Point out each Plasmodium parasite.
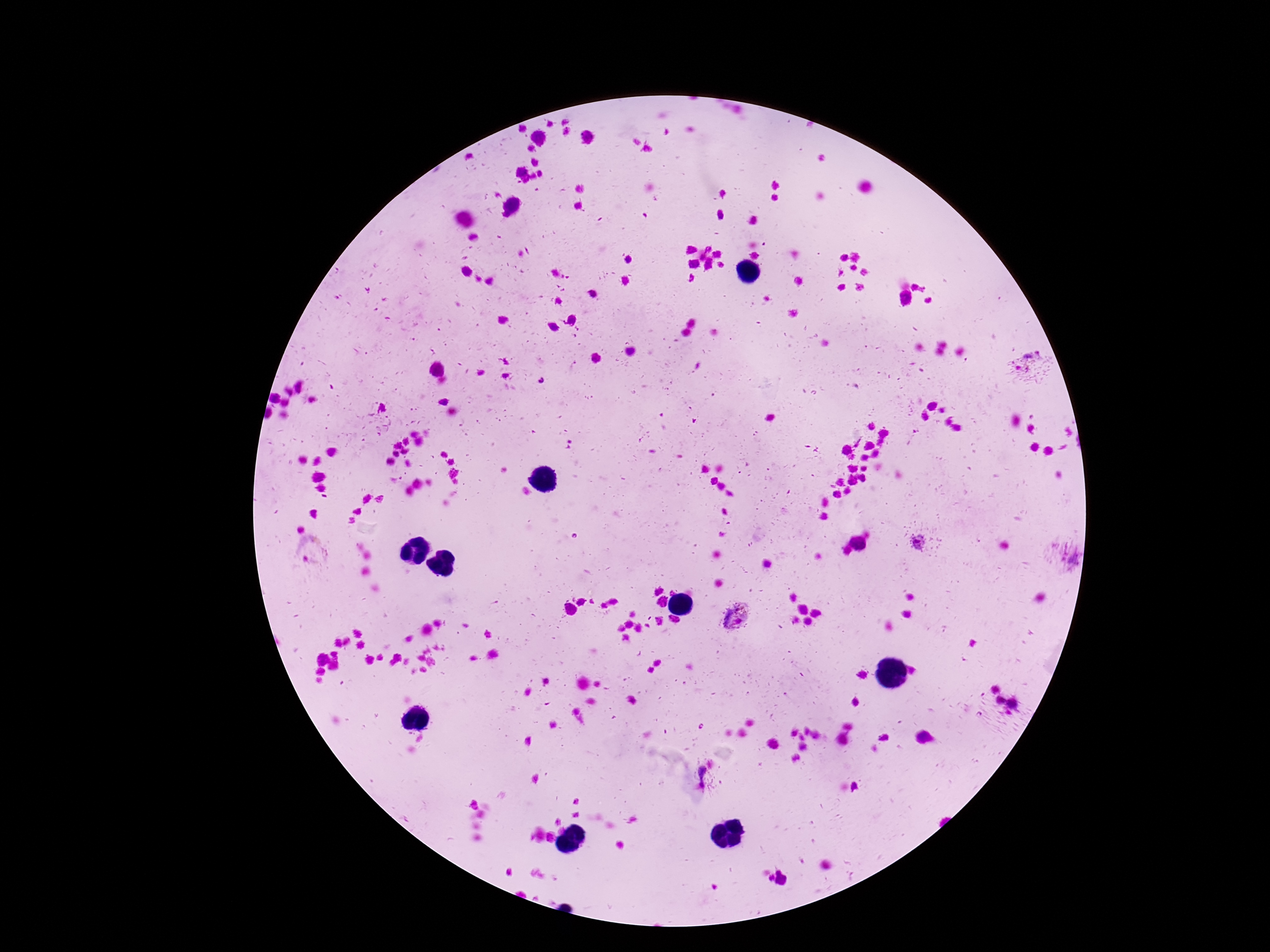

Approximate centers as (x, y) in pixels.
Plasmodium parasites: (1031, 365), (920, 542), (314, 555), (1073, 559), (734, 616).

Summary:
  - Patient malaria status: infected
  - Field of view: single
  - Capture: smartphone camera through the microscope eyepiece
  - Image size: 1270×952 pixels
  - Stain: Giemsa
  - Magnification: 100x
  - Preparation: thick blood smear